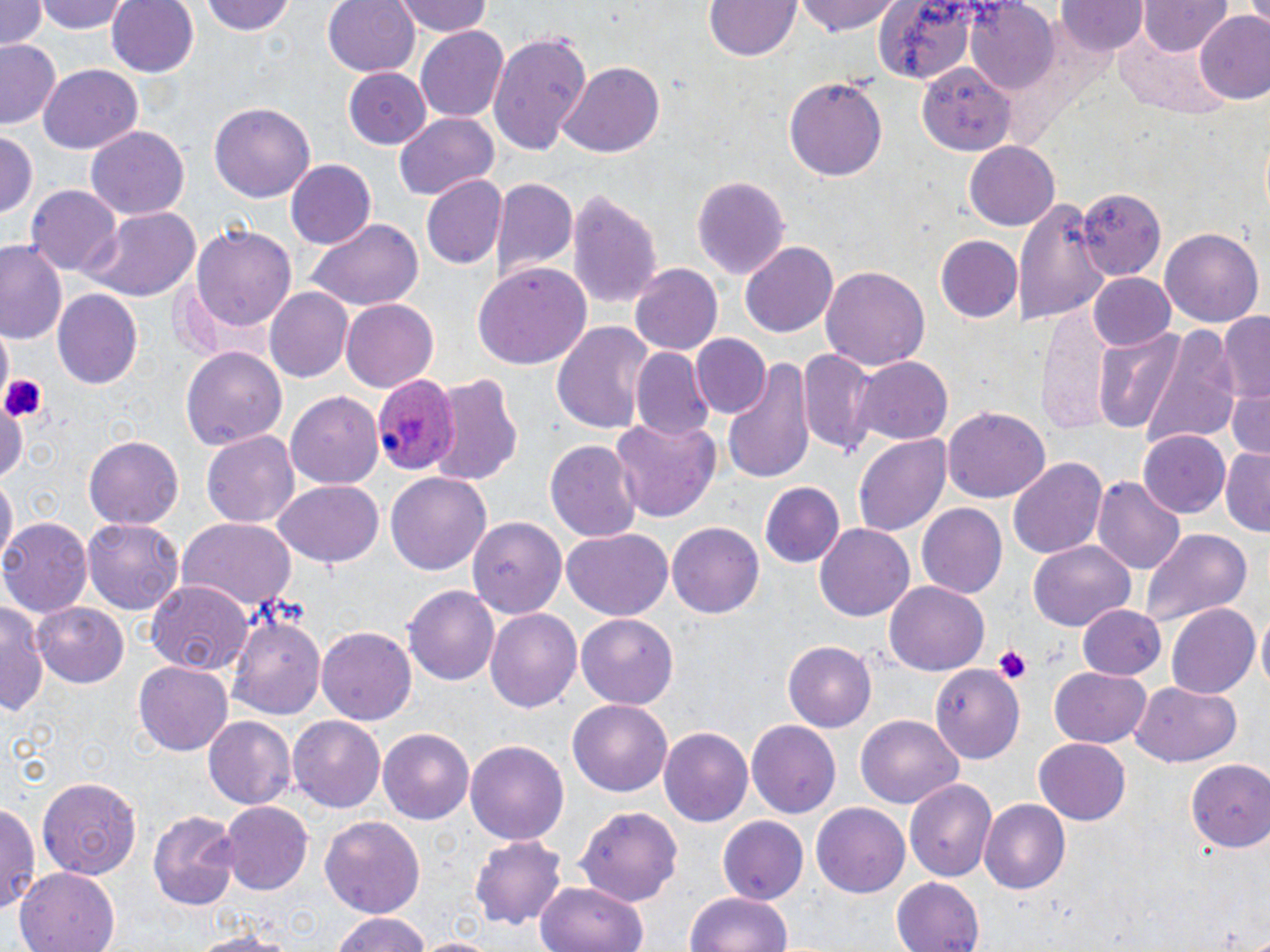

Summary:
  - Coordinate format: approximate bounding boxes as [x1, y1, x2, y2] in pixels
  - Uninfected red blood cell locations: [0, 0, 45, 50], [39, 0, 131, 34], [106, 0, 199, 77], [202, 0, 297, 37], [324, 0, 421, 76], [393, 0, 494, 38], [705, 0, 801, 61], [796, 0, 901, 36], [1137, 1, 1231, 55], [868, 2, 986, 81], [1058, 2, 1148, 55], [964, 4, 1057, 94], [1196, 14, 1270, 106], [416, 26, 511, 121], [487, 30, 590, 155], [0, 39, 63, 131], [558, 62, 663, 159], [37, 66, 141, 153], [915, 66, 1012, 153], [342, 68, 431, 150], [785, 78, 886, 182], [210, 100, 316, 203], [393, 110, 499, 202], [85, 127, 188, 221], [0, 130, 38, 217], [963, 141, 1059, 231], [284, 161, 374, 250], [422, 173, 508, 270], [692, 174, 788, 276], [490, 176, 577, 281], [566, 185, 663, 307], [28, 186, 120, 280], [1077, 191, 1165, 274], [1017, 196, 1107, 329], [80, 207, 202, 303], [304, 220, 421, 312], [191, 223, 296, 333], [1161, 226, 1263, 326], [935, 234, 1023, 323], [0, 239, 66, 345], [741, 241, 839, 337], [472, 264, 593, 369], [629, 264, 721, 357], [821, 266, 929, 370], [1088, 273, 1177, 351], [264, 285, 352, 381], [51, 288, 144, 389], [341, 299, 437, 392], [1036, 304, 1118, 430], [1219, 313, 1270, 407], [552, 321, 657, 438], [1135, 324, 1239, 451], [1092, 328, 1185, 432], [692, 333, 770, 418], [180, 343, 287, 449], [631, 347, 715, 442], [798, 347, 879, 458], [722, 355, 816, 485], [854, 355, 954, 446], [427, 373, 525, 487], [1228, 383, 1270, 460], [286, 392, 384, 488], [0, 400, 26, 488], [943, 407, 1049, 503], [612, 416, 723, 522], [201, 429, 300, 529], [1137, 431, 1230, 519], [83, 434, 184, 529], [853, 434, 951, 538], [545, 440, 643, 543], [1220, 446, 1270, 533], [1009, 456, 1107, 559], [385, 468, 491, 573], [0, 474, 16, 568], [1092, 475, 1184, 575], [273, 480, 384, 567], [758, 481, 844, 567], [915, 503, 1007, 600], [468, 514, 565, 618], [1, 518, 93, 616], [175, 518, 298, 612], [84, 519, 182, 616], [667, 521, 766, 618], [815, 521, 915, 619], [1138, 528, 1252, 623], [563, 530, 672, 620], [1028, 541, 1134, 630], [145, 581, 253, 678], [885, 581, 989, 674], [404, 583, 500, 684], [1, 597, 49, 717], [32, 602, 129, 689], [1166, 602, 1260, 698], [1078, 604, 1165, 680], [485, 608, 581, 716], [229, 612, 327, 720], [576, 614, 679, 709], [319, 625, 416, 726], [783, 642, 876, 731], [134, 661, 232, 756], [930, 662, 1023, 760], [1050, 666, 1151, 747], [1129, 682, 1241, 768], [568, 700, 671, 795], [204, 714, 295, 811], [855, 715, 965, 807], [288, 716, 386, 813], [748, 718, 843, 817], [659, 725, 753, 827], [379, 728, 474, 822], [1034, 738, 1131, 825], [466, 739, 568, 848], [1187, 759, 1270, 851], [38, 776, 141, 880], [905, 780, 1001, 878], [0, 797, 40, 915], [978, 800, 1069, 894], [219, 801, 311, 893], [813, 802, 910, 898], [577, 803, 685, 905], [148, 809, 241, 911], [321, 814, 425, 923], [719, 814, 808, 903], [470, 835, 567, 929], [16, 868, 121, 952], [890, 876, 984, 952], [537, 880, 647, 952], [686, 890, 792, 952], [328, 913, 433, 952], [182, 929, 304, 952]
  - Platelet locations: [2, 371, 46, 427], [993, 645, 1030, 684]
  - Plasmodium ovale-infected red blood cell locations: [374, 374, 460, 476]
  - Slide-level diagnosis: Plasmodium ovale
  - Image size: 1270×952 pixels
  - Stain: May-Grünwald-Giemsa
  - Modality: light microscopy
  - Preparation: thin blood smear
  - Field of view: single
  - Magnification: 1000x